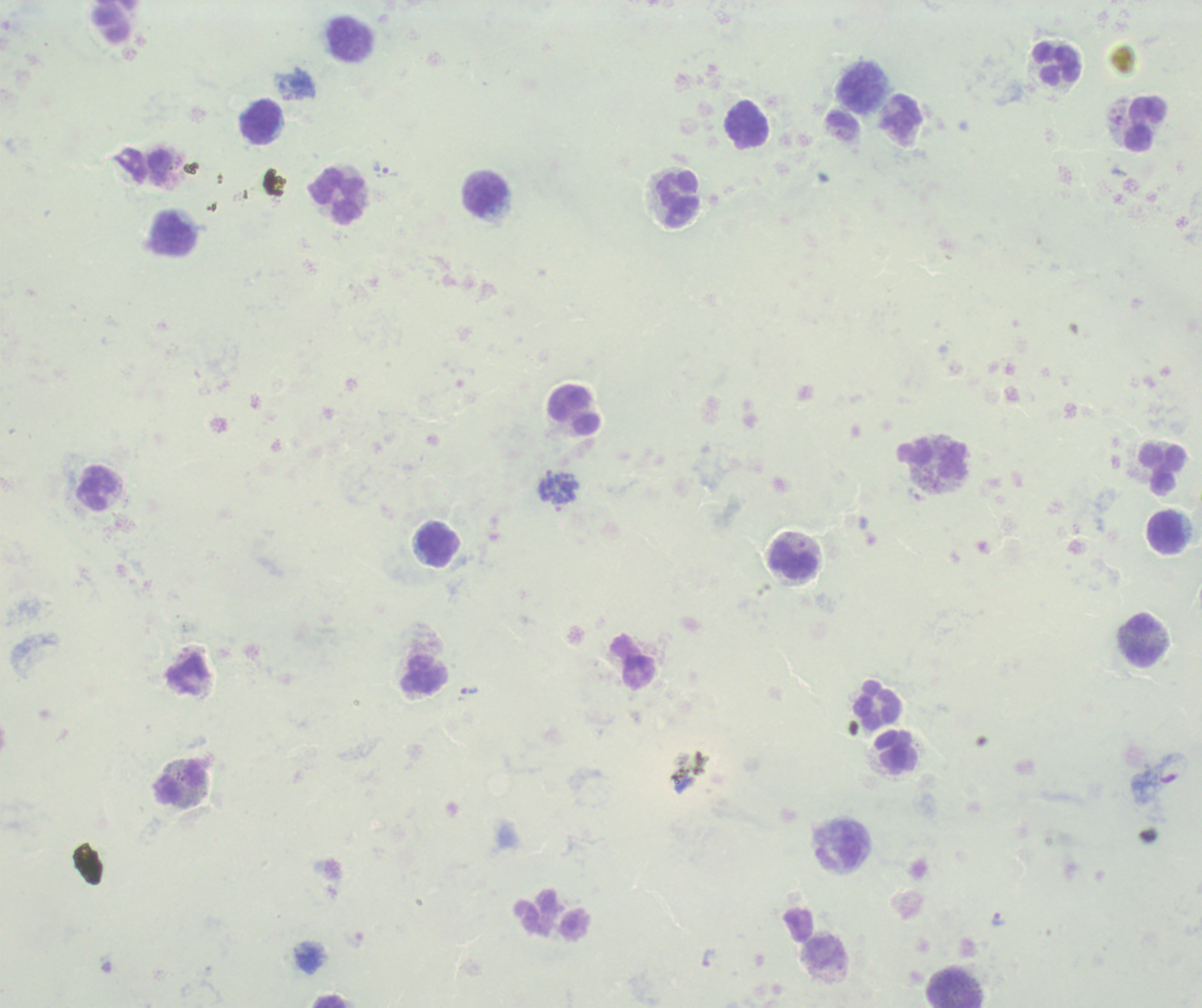

Approximate centers as [x, y] in pixels. Leukocyte locations: [350, 40], [1057, 64], [860, 86], [901, 116], [261, 121], [1146, 123], [747, 124], [486, 193], [336, 196], [678, 198], [173, 234], [933, 459], [1162, 468], [96, 488], [1167, 531], [438, 544], [794, 561], [1143, 639], [879, 703], [897, 751], [180, 784], [838, 845], [954, 995], [329, 1001]. Trophozoite locations: [385, 170], [470, 691], [999, 918], [353, 938], [709, 958]. Schizont locations: [559, 490]. Life-cycle stages observed: trophozoite, schizont. Image is 1202×1008 pixels. Background quality: unsatisfactory. Result: Plasmodium parasites detected. Thick blood film. 100x magnification. Previously used in an actual diagnosis. One field from this slide. Romanowsky-stained preparation.